Report the malaria status of this cell.
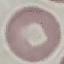

It is uninfected.

Thin blood film. Giemsa-stained preparation. Photographed with a smartphone camera at the microscope eyepiece. Cell patch, automatically extracted from a larger field of view and resized to 64 × 64 pixels.